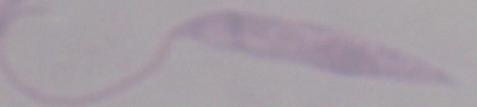

Summary:
  - Magnification: 1000x
  - Modality: micrograph
  - Identification: Leishmania